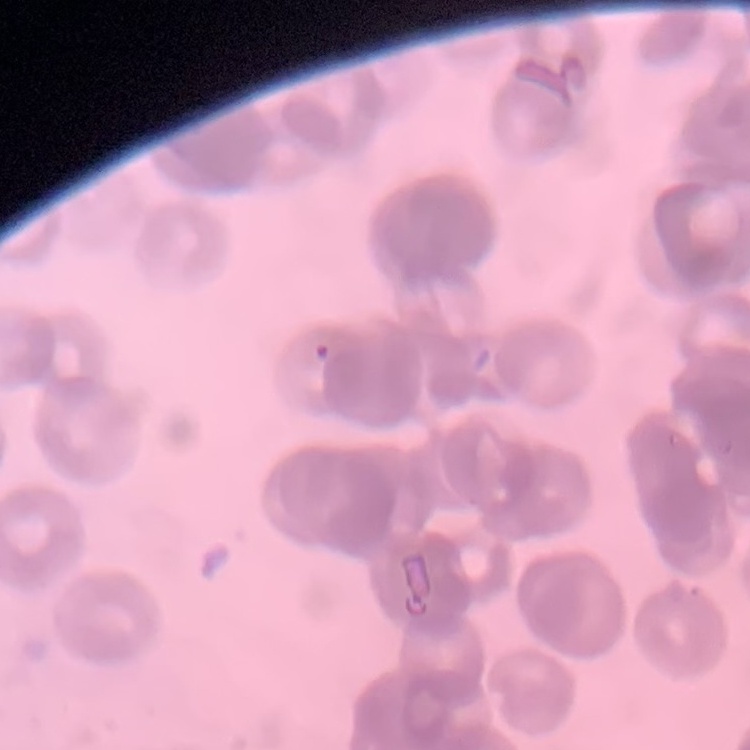

erythrocyte_morphology: rouleaux formation
stain: Field's or Giemsa
image_type: one tile cut from a larger photomicrograph
preparation: thin blood film